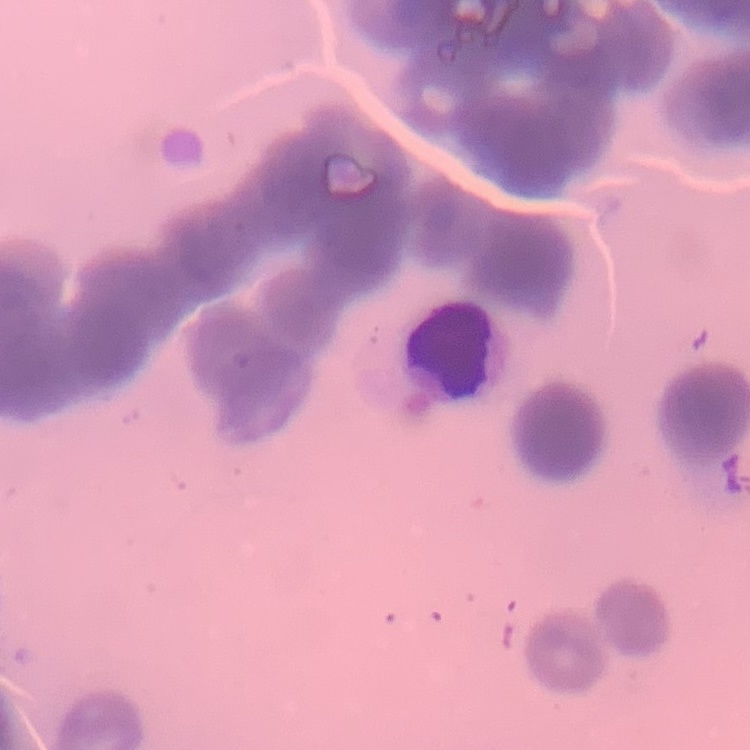
Summary:
  - Red blood cell morphology: rouleaux formation
  - Image type: one tile cut from a larger photomicrograph
  - Stain: Field's or Giemsa
  - Preparation: thin blood film